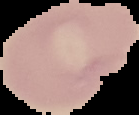
Image is 139×115 pixels. Result: negative for malaria parasites. Cell region segmented out of the field of view; the surrounding area is masked to black. From a thin blood smear.